Locate and identify every blood parasite.
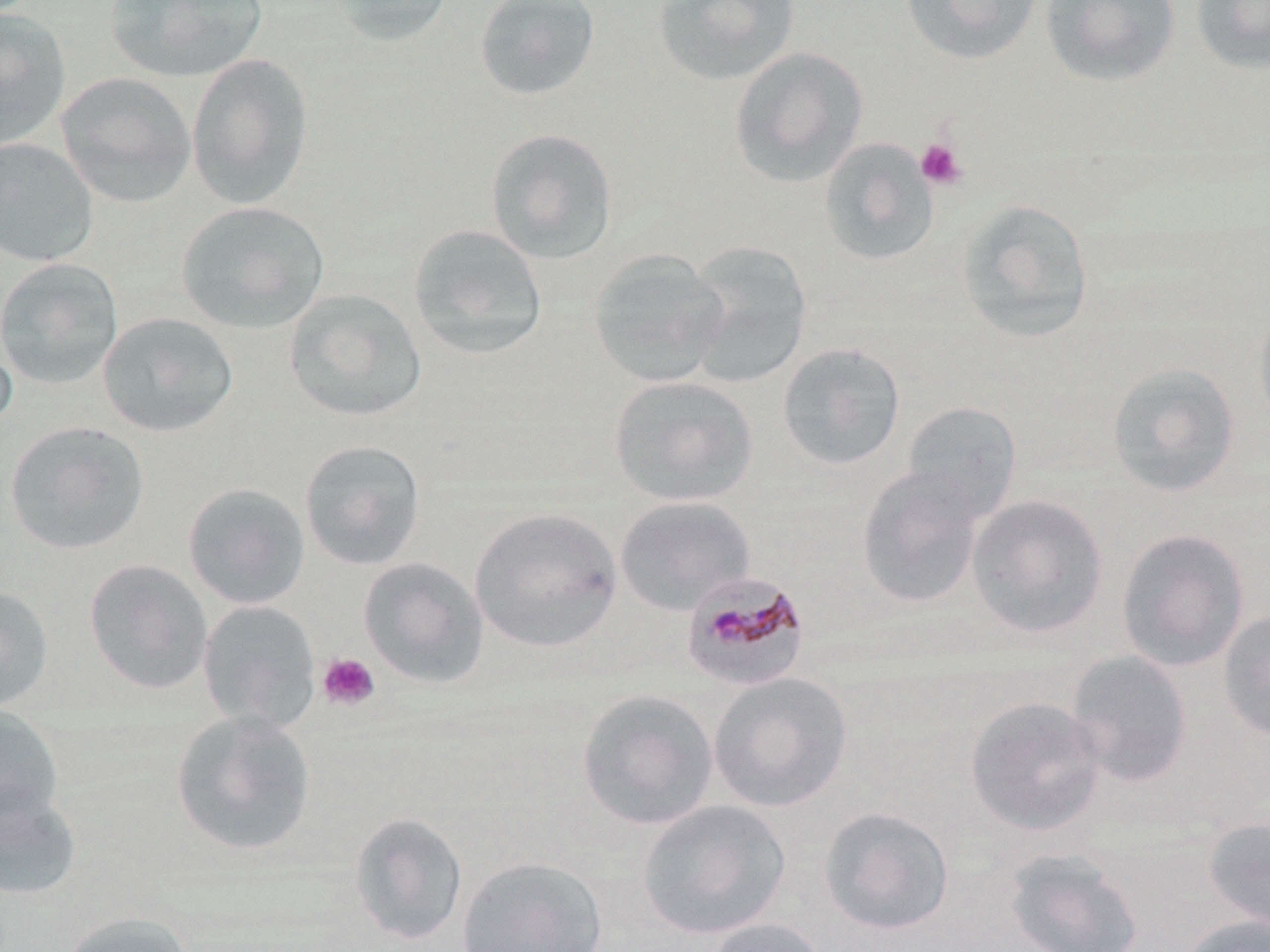
Approximate bounding boxes as [x1, y1, x2, y2] in pixels.
Plasmodium malariae-infected red blood cells: [681, 570, 811, 692].
No Plasmodium falciparum, Plasmodium ovale, Plasmodium vivax, Babesia divergens, or Trypanosoma brucei observed.

Uninfected red blood cell locations: [104, 0, 269, 83], [326, 0, 453, 47], [474, 0, 601, 102], [901, 0, 1042, 66], [1041, 0, 1180, 87], [1190, 0, 1270, 75], [653, 1, 800, 86], [0, 7, 72, 151], [729, 46, 869, 188], [186, 53, 314, 209], [55, 72, 196, 208], [485, 127, 619, 265], [0, 137, 99, 267], [818, 137, 940, 267], [956, 199, 1094, 344], [176, 201, 330, 334], [408, 224, 549, 361], [684, 242, 813, 389], [587, 249, 729, 387], [0, 258, 123, 390], [283, 289, 427, 422], [1254, 306, 1270, 429], [97, 312, 239, 438], [0, 324, 17, 440], [776, 342, 906, 471], [1106, 363, 1240, 498], [608, 375, 759, 507], [900, 401, 1022, 522], [4, 420, 150, 555], [298, 439, 427, 571], [856, 466, 987, 609], [182, 482, 311, 609], [966, 494, 1109, 639], [614, 495, 755, 615], [469, 507, 623, 654], [1115, 528, 1250, 672], [357, 557, 490, 690], [83, 559, 213, 695], [0, 585, 54, 710], [197, 599, 322, 734], [1218, 609, 1270, 741], [1065, 650, 1193, 786], [708, 671, 853, 813], [575, 688, 719, 831], [965, 695, 1106, 837], [0, 706, 64, 824], [170, 710, 317, 857], [0, 783, 83, 901], [637, 799, 791, 939], [819, 806, 955, 935], [348, 811, 469, 946], [1203, 816, 1270, 935], [1004, 847, 1144, 952], [456, 855, 608, 952], [59, 910, 194, 952], [1179, 914, 1270, 952], [705, 917, 830, 952]. Platelet locations: [915, 139, 967, 189], [317, 652, 380, 711]. Slide-level diagnosis: Plasmodium malariae. Single field of view. May-Grünwald-Giemsa stain. Thin blood film. Optical microscopy. Captured at 1000x magnification. Image is 1270×952 pixels.